Describe the morphology of the erythrocytes.
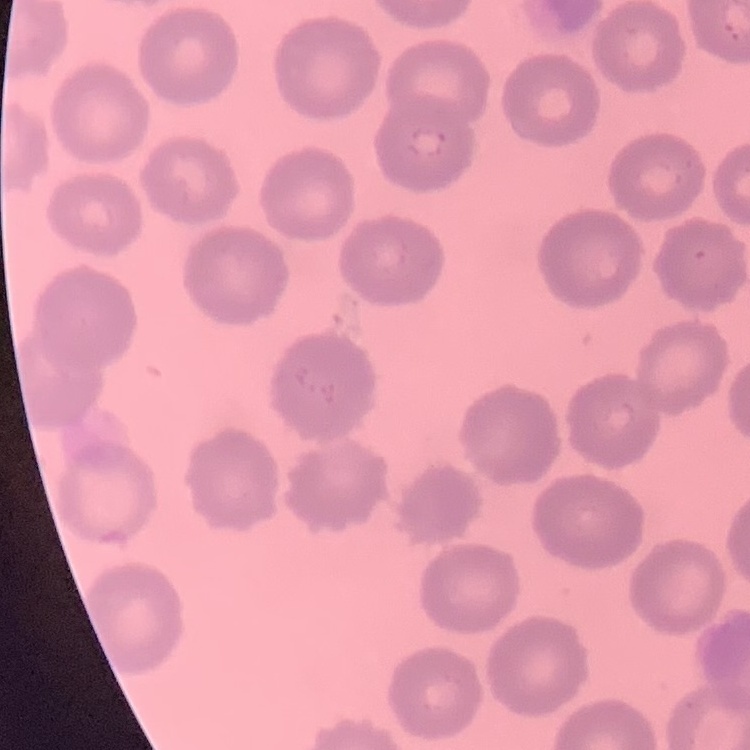
No rouleaux formation.

stain = Field's or Giemsa
image type = one tile cut from a larger photomicrograph
preparation = thin blood smear